Name the blood parasite species.
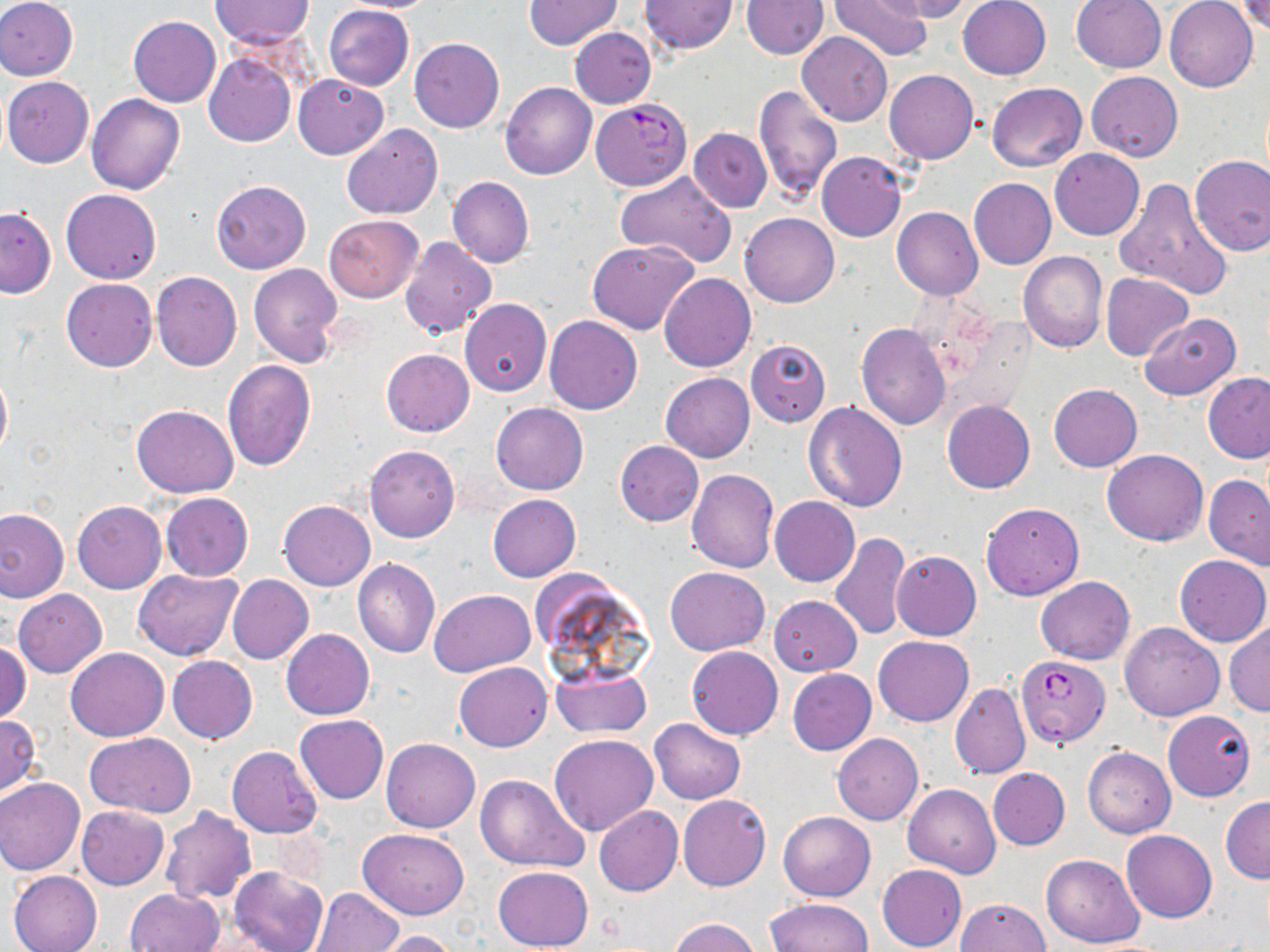
Plasmodium falciparum.

Summary:
  - Coordinate format: approximate bounding boxes as (x1,y1)-(x2,y2) corner pairs in pixels
  - Plasmodium falciparum-infected red blood cell locations: (589,99)-(691,191), (1016,656)-(1109,747)
  - Uninfected red blood cell locations: (0,0)-(78,81), (210,0)-(315,49), (333,0)-(447,12), (830,0)-(933,60), (882,0)-(978,22), (957,0)-(1051,80), (1071,0)-(1166,74), (1164,0)-(1257,92), (522,1)-(622,50), (640,1)-(737,54), (740,1)-(828,59), (1238,1)-(1269,37), (323,4)-(414,91), (128,16)-(221,108), (570,28)-(656,109), (797,31)-(892,126), (410,38)-(504,133), (204,53)-(296,147), (884,70)-(978,163), (1086,71)-(1183,161), (293,73)-(388,159), (2,77)-(93,169), (500,82)-(597,180), (986,82)-(1087,171), (753,86)-(843,202), (86,94)-(184,195), (341,124)-(443,218), (688,128)-(772,213), (1050,148)-(1144,240), (816,150)-(907,242), (1190,155)-(1270,257), (615,170)-(738,268), (447,176)-(534,267), (1113,177)-(1233,302), (969,178)-(1056,270), (211,179)-(311,274), (61,188)-(161,284), (0,207)-(56,297), (892,207)-(984,300), (740,212)-(839,308), (324,215)-(423,303), (400,237)-(497,338), (587,239)-(701,336), (1018,251)-(1108,353), (249,263)-(343,367), (151,272)-(242,371), (659,273)-(756,372), (1101,273)-(1193,360), (61,278)-(157,372), (459,299)-(552,396), (452,307)-(640,403), (1138,312)-(1241,401), (544,315)-(643,415), (857,323)-(952,430), (746,340)-(831,426), (382,349)-(474,437), (223,360)-(315,471), (0,367)-(12,460), (1202,372)-(1270,463), (661,373)-(754,462), (1049,384)-(1142,472), (942,400)-(1034,495), (802,401)-(908,512), (491,402)-(588,494), (131,404)-(238,497), (615,441)-(704,525), (364,445)-(460,543), (1102,449)-(1207,546), (687,468)-(779,572), (1204,474)-(1270,568), (161,493)-(253,581), (488,494)-(581,582), (770,496)-(860,587), (73,500)-(166,593), (278,500)-(375,590), (981,502)-(1084,600), (0,507)-(69,603), (829,532)-(911,640), (892,550)-(981,640), (1175,556)-(1270,647), (353,559)-(442,658), (665,567)-(770,655), (132,570)-(241,661), (227,575)-(314,664), (1036,576)-(1134,664), (13,588)-(107,678), (430,589)-(535,675), (769,595)-(861,676), (1119,621)-(1225,721), (1225,621)-(1270,718), (281,629)-(374,720), (874,635)-(973,725), (0,640)-(31,726), (687,646)-(782,739), (66,647)-(168,741), (167,655)-(257,745), (455,662)-(552,751), (552,663)-(651,738), (786,668)-(876,755), (950,681)-(1031,780), (1163,710)-(1255,801), (294,714)-(388,803), (0,715)-(41,796), (649,718)-(745,804), (85,732)-(195,817), (832,733)-(923,826), (549,735)-(660,837), (382,739)-(480,833), (227,746)-(322,838), (1083,747)-(1175,838), (988,767)-(1070,850), (475,774)-(589,871), (0,778)-(84,876), (903,783)-(1000,877), (678,794)-(771,891), (1220,797)-(1270,883), (76,805)-(169,889), (594,806)-(683,896), (159,807)-(256,905), (778,811)-(876,900), (358,827)-(470,919), (1122,831)-(1217,923), (1040,853)-(1145,948), (877,865)-(967,952), (231,866)-(328,952), (493,866)-(593,952), (7,869)-(102,952), (125,887)-(224,952), (311,887)-(404,952), (767,898)-(872,952), (956,898)-(1050,952), (668,917)-(761,952), (374,930)-(461,952)
  - Field of view: single
  - Magnification: 1000x
  - Preparation: thin blood film
  - Stain: May-Grünwald-Giemsa
  - Image size: 1270×952 pixels
  - Modality: optical microscopy